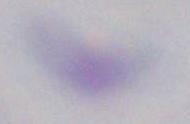

modality = photomicrograph
identification = Toxoplasma gondii
magnification = 1000x